State which cell type is depicted.
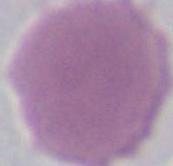

This is an erythrocyte.

Captured at 1000x magnification. Photomicrograph.